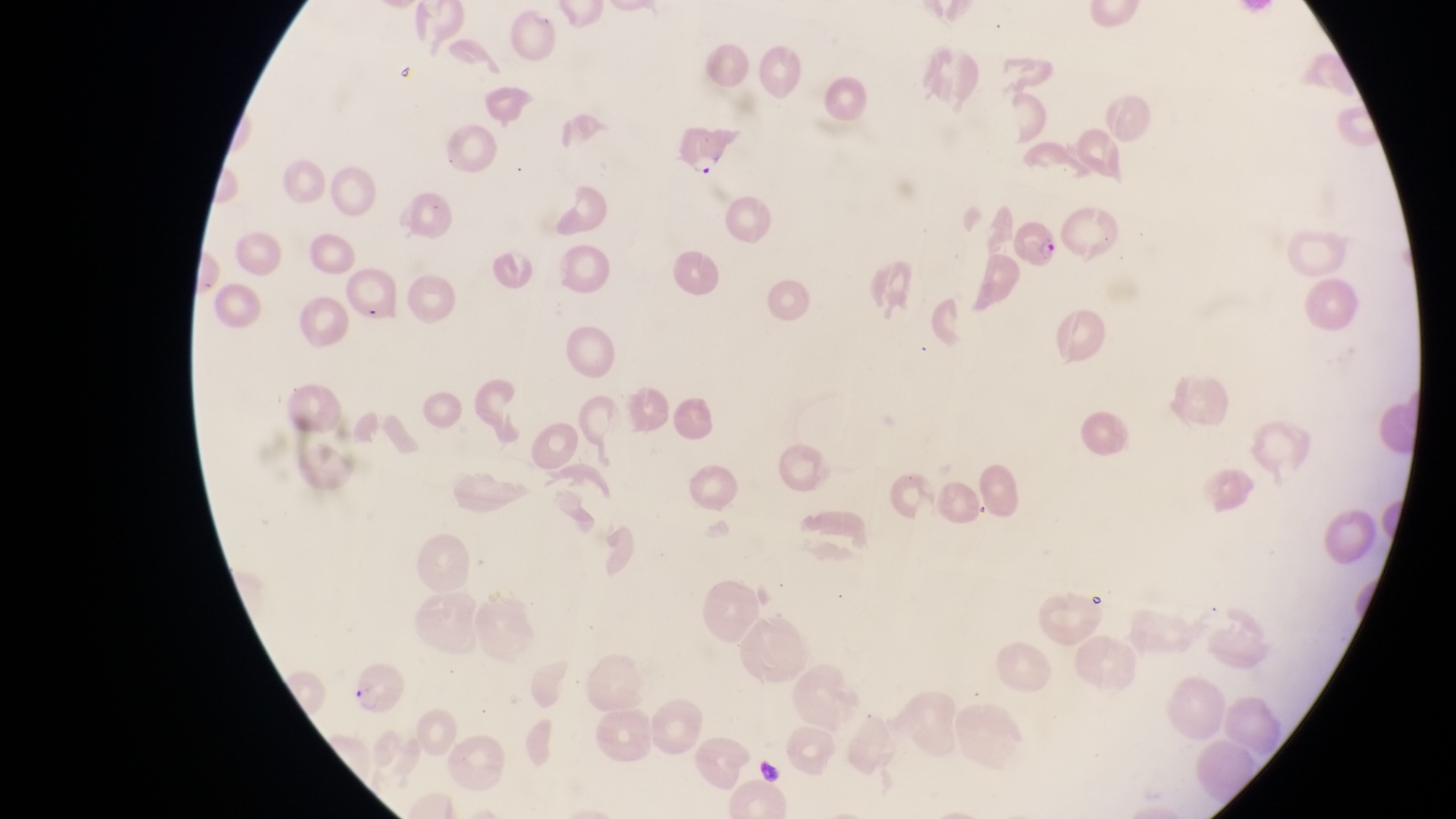
Approximate bounding boxes as {left, top, right, bottom} in pixels.
Summary:
  - Artifact (platelet-like body, stain precipitate, or debris) locations: {753, 755, 786, 789}
  - Parasitised red blood cell locations: {674, 124, 733, 183}, {1012, 217, 1064, 270}, {343, 271, 402, 329}, {343, 661, 412, 714}
  - Country: Uganda
  - Magnification: 1000x
  - Image size: 1456×819 pixels
  - Capture: smartphone photograph through the eyepiece of an Olympus CX-23 microscope
  - Field of view: single
  - Preparation: thin blood film